Assess for malaria.
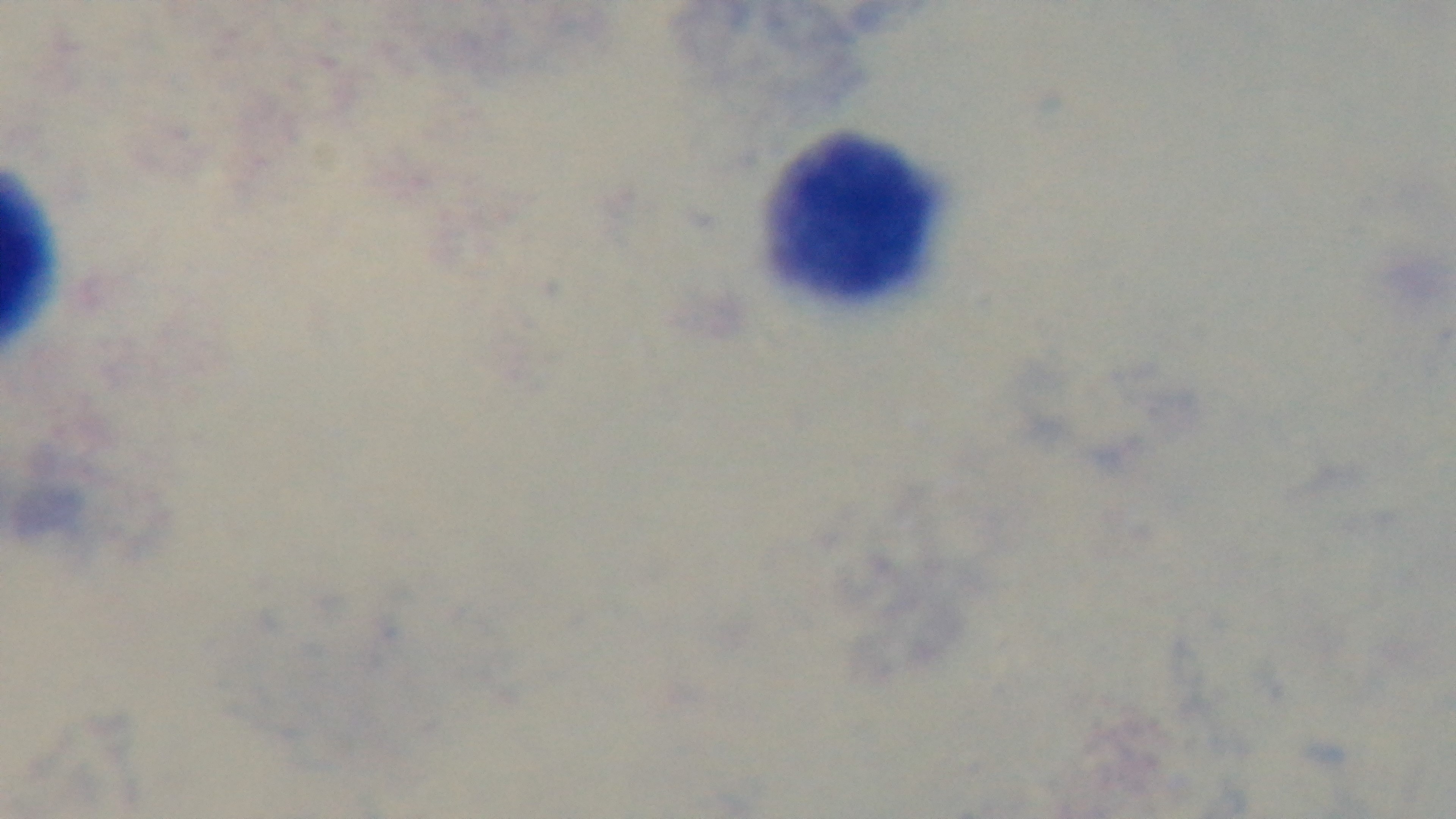
It is uninfected.

{
  "stain": "Giemsa",
  "preparation": "thick",
  "capture": "mounted 4K digital camera",
  "objective": "100x oil immersion",
  "field_of_view": "one from the slide",
  "modality": "light microscopy"
}